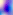
Micrograph. Captured at 400x magnification. Toxoplasma gondii is seen.